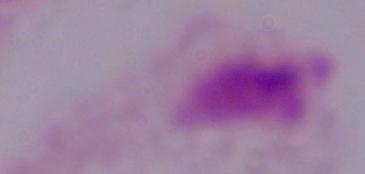

Summary:
  - Modality: micrograph
  - Identification: trichomonad
  - Magnification: 1000x